Give the extent of all Plasmodium vivax-infected red blood cells.
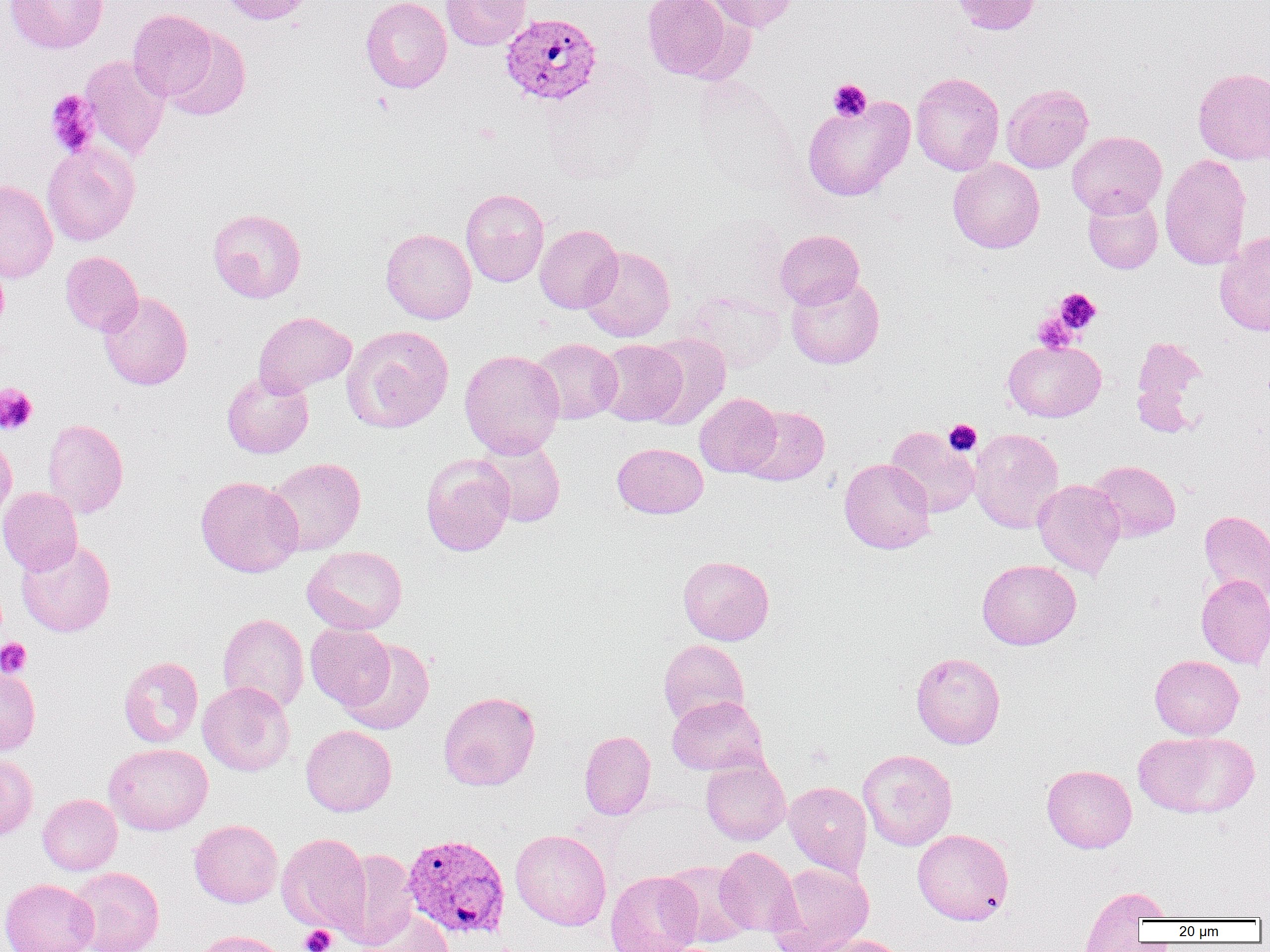

Approximate bounding boxes as named x1/y1/x2/y2 corners in pixels.
Plasmodium vivax-infected red blood cells: (x1=500, y1=12, x2=603, y2=106), (x1=400, y1=844, x2=508, y2=941).

Platelet locations: (x1=828, y1=79, x2=872, y2=121), (x1=45, y1=90, x2=100, y2=157), (x1=1053, y1=288, x2=1101, y2=335), (x1=1032, y1=312, x2=1079, y2=353), (x1=0, y1=384, x2=37, y2=435), (x1=944, y1=419, x2=982, y2=456), (x1=0, y1=638, x2=32, y2=678), (x1=300, y1=925, x2=336, y2=952). Uninfected red blood cell locations: (x1=5, y1=0, x2=108, y2=53), (x1=218, y1=0, x2=313, y2=25), (x1=360, y1=0, x2=452, y2=93), (x1=441, y1=0, x2=531, y2=50), (x1=642, y1=0, x2=739, y2=82), (x1=705, y1=0, x2=800, y2=33), (x1=949, y1=0, x2=1041, y2=34), (x1=128, y1=9, x2=217, y2=101), (x1=162, y1=27, x2=251, y2=121), (x1=79, y1=54, x2=171, y2=161), (x1=1193, y1=67, x2=1270, y2=164), (x1=910, y1=72, x2=1005, y2=175), (x1=1001, y1=83, x2=1093, y2=173), (x1=802, y1=95, x2=915, y2=202), (x1=1067, y1=130, x2=1166, y2=218), (x1=41, y1=142, x2=139, y2=245), (x1=1159, y1=153, x2=1253, y2=270), (x1=948, y1=158, x2=1044, y2=253), (x1=0, y1=180, x2=58, y2=283), (x1=461, y1=188, x2=549, y2=287), (x1=1082, y1=192, x2=1163, y2=274), (x1=207, y1=208, x2=306, y2=303), (x1=535, y1=224, x2=622, y2=313), (x1=381, y1=228, x2=476, y2=324), (x1=775, y1=229, x2=864, y2=309), (x1=1214, y1=232, x2=1270, y2=336), (x1=580, y1=246, x2=675, y2=342), (x1=60, y1=251, x2=143, y2=335), (x1=785, y1=274, x2=885, y2=369), (x1=679, y1=289, x2=787, y2=372), (x1=98, y1=292, x2=193, y2=390), (x1=253, y1=311, x2=356, y2=396), (x1=342, y1=325, x2=454, y2=434), (x1=644, y1=333, x2=731, y2=430), (x1=1131, y1=335, x2=1207, y2=433), (x1=530, y1=338, x2=622, y2=424), (x1=595, y1=338, x2=687, y2=425), (x1=1003, y1=340, x2=1106, y2=422), (x1=459, y1=349, x2=565, y2=458), (x1=222, y1=370, x2=314, y2=458), (x1=695, y1=393, x2=782, y2=477), (x1=740, y1=405, x2=829, y2=485), (x1=42, y1=418, x2=128, y2=518), (x1=886, y1=426, x2=980, y2=518), (x1=969, y1=427, x2=1063, y2=533), (x1=0, y1=434, x2=18, y2=523), (x1=476, y1=437, x2=566, y2=528), (x1=612, y1=442, x2=708, y2=519), (x1=421, y1=453, x2=515, y2=556), (x1=265, y1=457, x2=366, y2=555), (x1=839, y1=458, x2=935, y2=553), (x1=1087, y1=460, x2=1181, y2=542), (x1=196, y1=476, x2=303, y2=577), (x1=1032, y1=479, x2=1125, y2=578), (x1=0, y1=487, x2=83, y2=575), (x1=1199, y1=510, x2=1270, y2=603), (x1=16, y1=539, x2=116, y2=637), (x1=302, y1=545, x2=407, y2=634), (x1=678, y1=555, x2=774, y2=645), (x1=977, y1=559, x2=1081, y2=649), (x1=1196, y1=574, x2=1270, y2=668), (x1=218, y1=613, x2=309, y2=713), (x1=305, y1=623, x2=395, y2=711), (x1=340, y1=639, x2=434, y2=735), (x1=658, y1=639, x2=749, y2=727), (x1=911, y1=651, x2=1006, y2=749), (x1=1150, y1=655, x2=1244, y2=740), (x1=118, y1=656, x2=203, y2=748), (x1=0, y1=666, x2=41, y2=755), (x1=198, y1=681, x2=295, y2=776), (x1=438, y1=691, x2=540, y2=791), (x1=667, y1=695, x2=768, y2=775), (x1=300, y1=725, x2=396, y2=816), (x1=579, y1=730, x2=655, y2=819), (x1=1133, y1=731, x2=1260, y2=818), (x1=104, y1=743, x2=213, y2=835), (x1=858, y1=749, x2=957, y2=851), (x1=0, y1=754, x2=38, y2=842), (x1=700, y1=756, x2=791, y2=845), (x1=1041, y1=764, x2=1137, y2=853), (x1=783, y1=781, x2=872, y2=876), (x1=37, y1=794, x2=122, y2=875), (x1=189, y1=819, x2=283, y2=907), (x1=510, y1=829, x2=611, y2=930), (x1=912, y1=829, x2=1014, y2=925), (x1=277, y1=833, x2=371, y2=933), (x1=714, y1=846, x2=800, y2=935), (x1=332, y1=849, x2=419, y2=949), (x1=660, y1=860, x2=752, y2=948), (x1=766, y1=862, x2=874, y2=952), (x1=68, y1=867, x2=164, y2=952), (x1=605, y1=871, x2=702, y2=952), (x1=0, y1=878, x2=99, y2=952), (x1=1079, y1=885, x2=1169, y2=950), (x1=358, y1=906, x2=454, y2=952), (x1=194, y1=930, x2=291, y2=952), (x1=809, y1=935, x2=908, y2=952). Slide-level diagnosis: Plasmodium vivax. Single field of view. Thin blood film. Image is 1270×952 pixels. Captured at 1000x magnification. Optical microscopy.